Point out Plasmodium parasites and leukocytes.
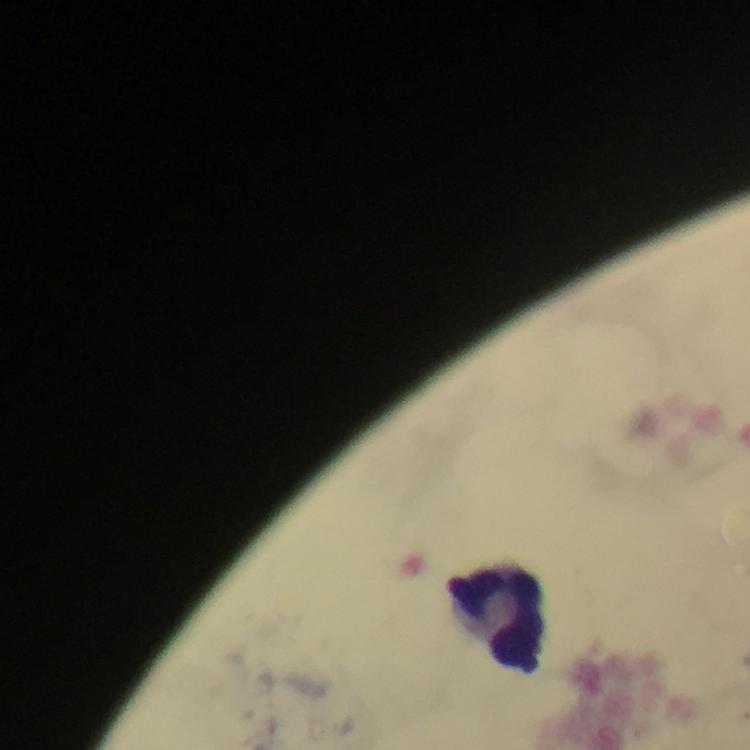
No Plasmodium parasites detected.
Approximate centers as {x, y} in pixels.
Leukocytes: {495, 620}.

Giemsa stain. 100x magnification. Immersion oil was used. From a malaria diagnostic workup. Cropped region of a single field of view. Photographed with a smartphone mounted on the microscope. Thick blood smear. Image is 750×750 pixels.